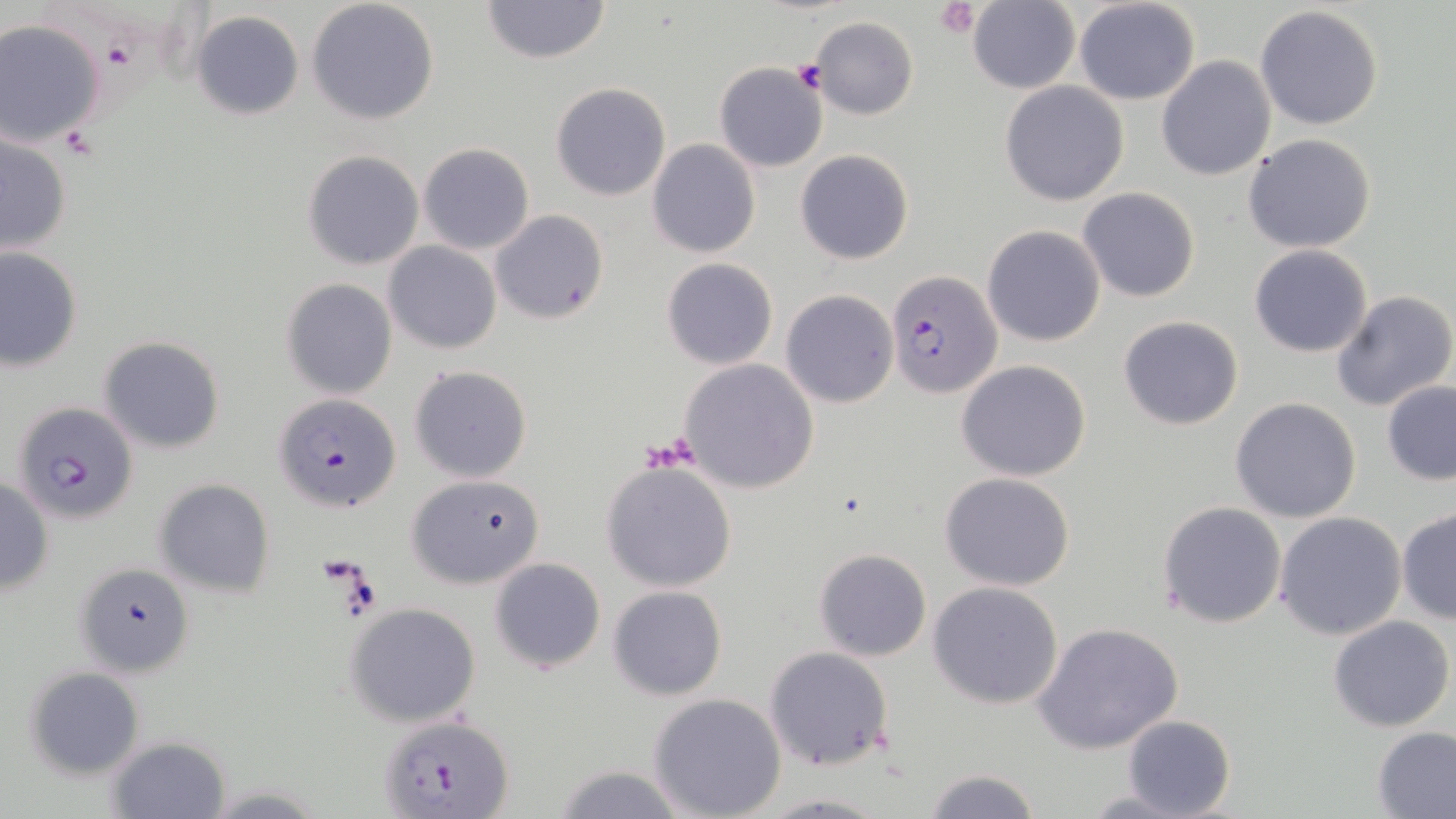

Approximate bounding boxes as (x1,y1)-(x2,y2) corner pairs in pixels. Uninfected red blood cell locations: (305,0)-(441,124), (481,0)-(612,64), (1073,0)-(1201,105), (968,2)-(1080,95), (1254,6)-(1385,131), (189,9)-(305,121), (809,17)-(919,120), (1,19)-(106,146), (1156,55)-(1276,181), (714,61)-(829,171), (999,80)-(1129,206), (551,82)-(672,200), (0,132)-(73,259), (1243,133)-(1378,254), (648,138)-(760,257), (418,142)-(534,255), (795,149)-(914,265), (302,150)-(424,270), (1077,187)-(1200,302), (490,209)-(609,325), (982,225)-(1106,347), (385,242)-(501,353), (1248,245)-(1373,356), (0,247)-(83,371), (661,258)-(779,370), (281,277)-(397,399), (1331,289)-(1456,411), (780,290)-(898,408), (1117,315)-(1243,429), (99,336)-(226,454), (679,359)-(819,494), (956,360)-(1093,481), (408,364)-(532,482), (1381,379)-(1456,486), (1230,397)-(1362,524), (602,460)-(737,592), (405,472)-(548,590), (940,473)-(1074,591), (0,477)-(55,595), (152,478)-(277,598), (1158,500)-(1287,628), (1397,509)-(1456,625), (1275,512)-(1407,641), (813,548)-(932,661), (489,557)-(606,674), (76,560)-(194,679), (928,582)-(1063,708), (607,586)-(727,700), (344,602)-(481,727), (1328,615)-(1454,732), (1034,622)-(1183,756), (763,645)-(895,771), (24,666)-(146,778), (647,692)-(788,819), (1120,714)-(1236,819), (1372,725)-(1456,818), (106,735)-(231,817), (551,764)-(689,819), (924,767)-(1040,819), (1083,791)-(1193,817), (757,792)-(894,817). Plasmodium falciparum-infected red blood cell locations: (885,269)-(1003,399), (275,392)-(401,515), (12,400)-(138,524), (378,715)-(514,818). Platelet locations: (937,1)-(980,38), (792,62)-(827,93), (57,125)-(100,159). Slide-level diagnosis: Plasmodium falciparum. Image is 1456×819 pixels. Light microscopy. Single field of view. May-Grünwald-Giemsa-stained preparation. 1000x magnification. Thin blood film.